Outline each uninfected red blood cell.
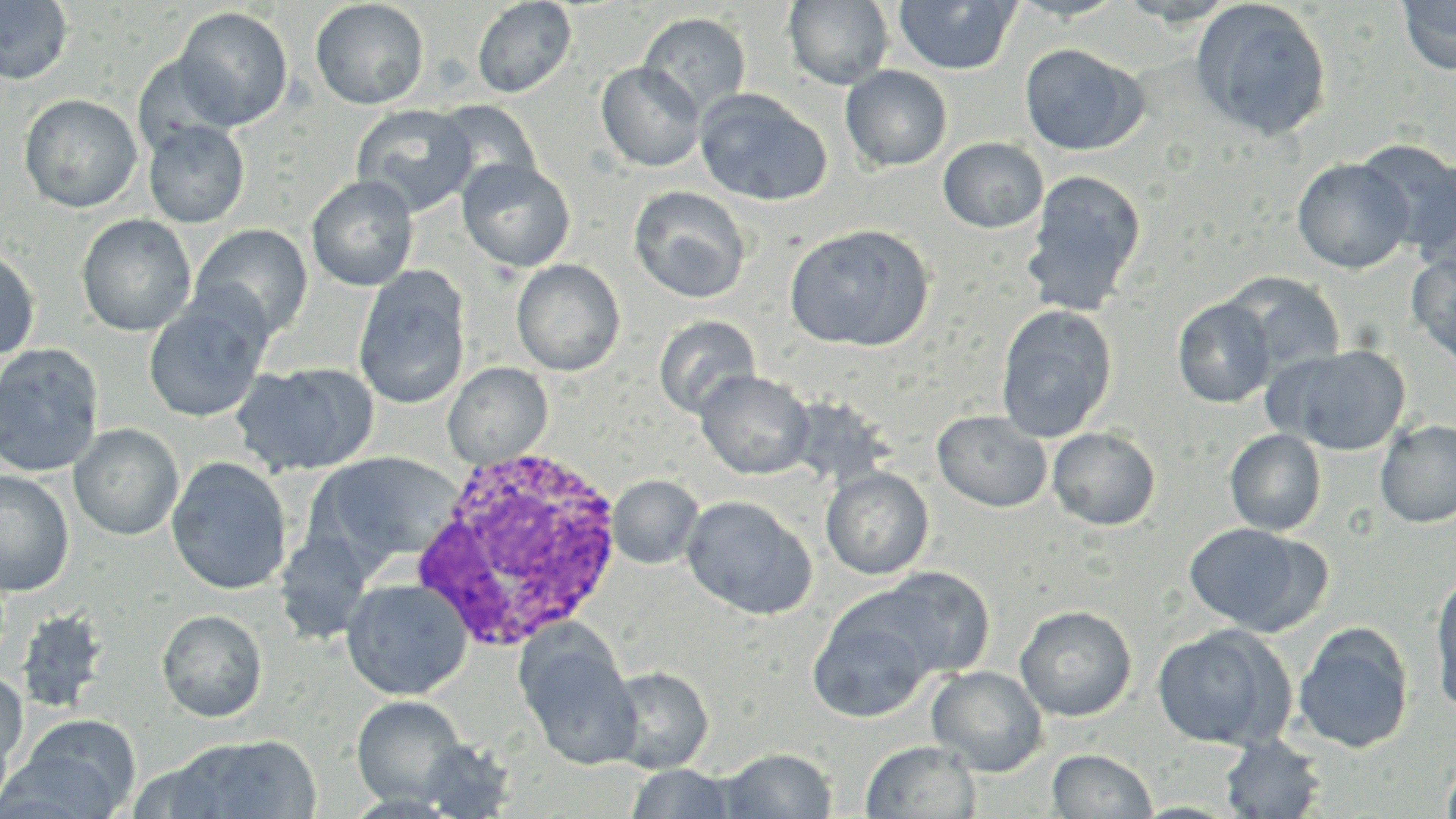
Approximate bounding boxes as named x1/y1/x2/y2 corners in pixels.
Uninfected red blood cells: (x1=783, y1=0, x2=894, y2=90), (x1=893, y1=0, x2=1020, y2=76), (x1=1397, y1=0, x2=1456, y2=76), (x1=0, y1=1, x2=74, y2=85), (x1=309, y1=1, x2=429, y2=110), (x1=472, y1=1, x2=577, y2=98), (x1=1191, y1=1, x2=1333, y2=142), (x1=173, y1=6, x2=293, y2=131), (x1=638, y1=12, x2=752, y2=118), (x1=1020, y1=43, x2=1145, y2=156), (x1=133, y1=55, x2=235, y2=159), (x1=596, y1=62, x2=705, y2=172), (x1=840, y1=65, x2=952, y2=172), (x1=695, y1=89, x2=832, y2=206), (x1=18, y1=94, x2=142, y2=213), (x1=433, y1=99, x2=542, y2=195), (x1=351, y1=104, x2=478, y2=216), (x1=143, y1=120, x2=250, y2=228), (x1=938, y1=137, x2=1049, y2=234), (x1=1371, y1=142, x2=1456, y2=267), (x1=1292, y1=157, x2=1414, y2=274), (x1=457, y1=158, x2=576, y2=273), (x1=1022, y1=169, x2=1147, y2=316), (x1=306, y1=174, x2=418, y2=291), (x1=628, y1=186, x2=751, y2=304), (x1=76, y1=214, x2=197, y2=336), (x1=783, y1=222, x2=934, y2=352), (x1=189, y1=224, x2=313, y2=341), (x1=0, y1=245, x2=41, y2=362), (x1=1407, y1=251, x2=1456, y2=368), (x1=511, y1=259, x2=626, y2=376), (x1=353, y1=267, x2=471, y2=410), (x1=1223, y1=273, x2=1347, y2=375), (x1=142, y1=293, x2=271, y2=423), (x1=1173, y1=297, x2=1277, y2=408), (x1=995, y1=304, x2=1118, y2=442), (x1=653, y1=315, x2=761, y2=419), (x1=0, y1=344, x2=105, y2=478), (x1=1275, y1=344, x2=1411, y2=456), (x1=443, y1=361, x2=553, y2=468), (x1=231, y1=362, x2=379, y2=477), (x1=695, y1=369, x2=814, y2=480), (x1=932, y1=410, x2=1051, y2=512), (x1=1374, y1=418, x2=1456, y2=528), (x1=68, y1=424, x2=184, y2=541), (x1=1047, y1=427, x2=1161, y2=531), (x1=1224, y1=429, x2=1327, y2=536), (x1=312, y1=452, x2=460, y2=567), (x1=166, y1=457, x2=292, y2=595), (x1=820, y1=467, x2=934, y2=580), (x1=0, y1=470, x2=75, y2=597), (x1=607, y1=475, x2=703, y2=569), (x1=681, y1=495, x2=817, y2=619), (x1=1183, y1=522, x2=1322, y2=635), (x1=274, y1=532, x2=377, y2=644), (x1=872, y1=567, x2=996, y2=679), (x1=1430, y1=569, x2=1456, y2=714), (x1=341, y1=578, x2=473, y2=700), (x1=807, y1=594, x2=941, y2=723), (x1=1015, y1=604, x2=1137, y2=721), (x1=14, y1=607, x2=111, y2=715), (x1=156, y1=609, x2=268, y2=722), (x1=1293, y1=622, x2=1415, y2=753), (x1=1151, y1=623, x2=1295, y2=750), (x1=517, y1=632, x2=642, y2=768), (x1=926, y1=665, x2=1048, y2=776), (x1=606, y1=666, x2=714, y2=774), (x1=0, y1=670, x2=28, y2=775), (x1=351, y1=696, x2=466, y2=806), (x1=11, y1=714, x2=141, y2=818), (x1=0, y1=717, x2=15, y2=816), (x1=170, y1=734, x2=323, y2=819), (x1=1220, y1=734, x2=1327, y2=818), (x1=416, y1=738, x2=519, y2=818), (x1=860, y1=740, x2=982, y2=819), (x1=718, y1=747, x2=837, y2=818), (x1=1048, y1=748, x2=1158, y2=818), (x1=1440, y1=751, x2=1456, y2=819), (x1=125, y1=757, x2=232, y2=818), (x1=625, y1=764, x2=739, y2=818).

White blood cell locations: (x1=408, y1=442, x2=630, y2=651). Slide-level diagnosis: Plasmodium ovale. One field of a larger specimen. Captured at 1000x magnification. Image is 1456×819 pixels. May-Grünwald-Giemsa-stained preparation. Light microscopy. Thin blood film.